Assess this cell for malaria.
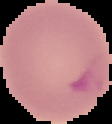
Parasitized.

image_type: segmented cell region with the area outside set to black
image_size: 112×124 pixels
preparation: thin blood film